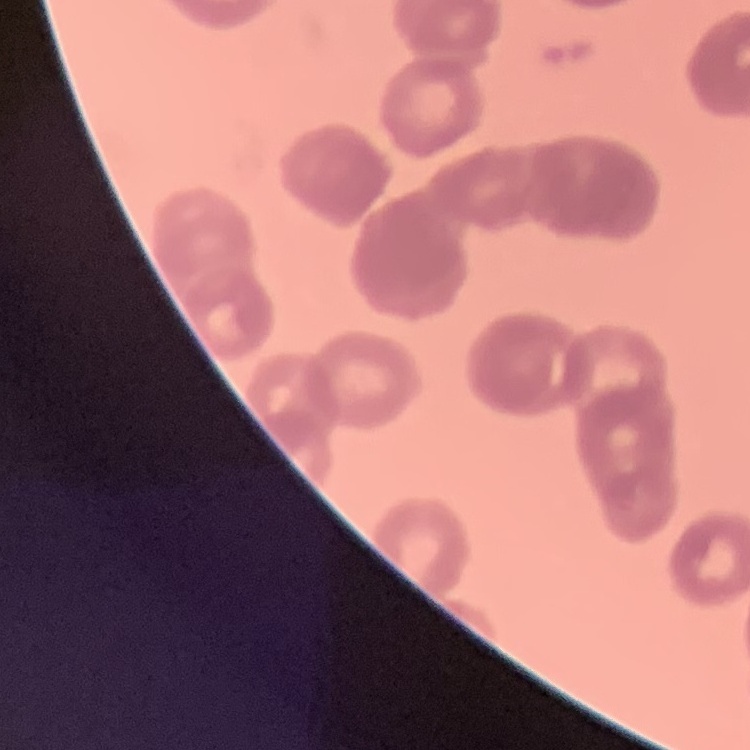
The erythrocytes exhibit rouleaux formation. Thin blood film. Stained with either Field's or Giemsa. Square crop of a larger photomicrograph.